Give a bounding box for every leukocyte visible.
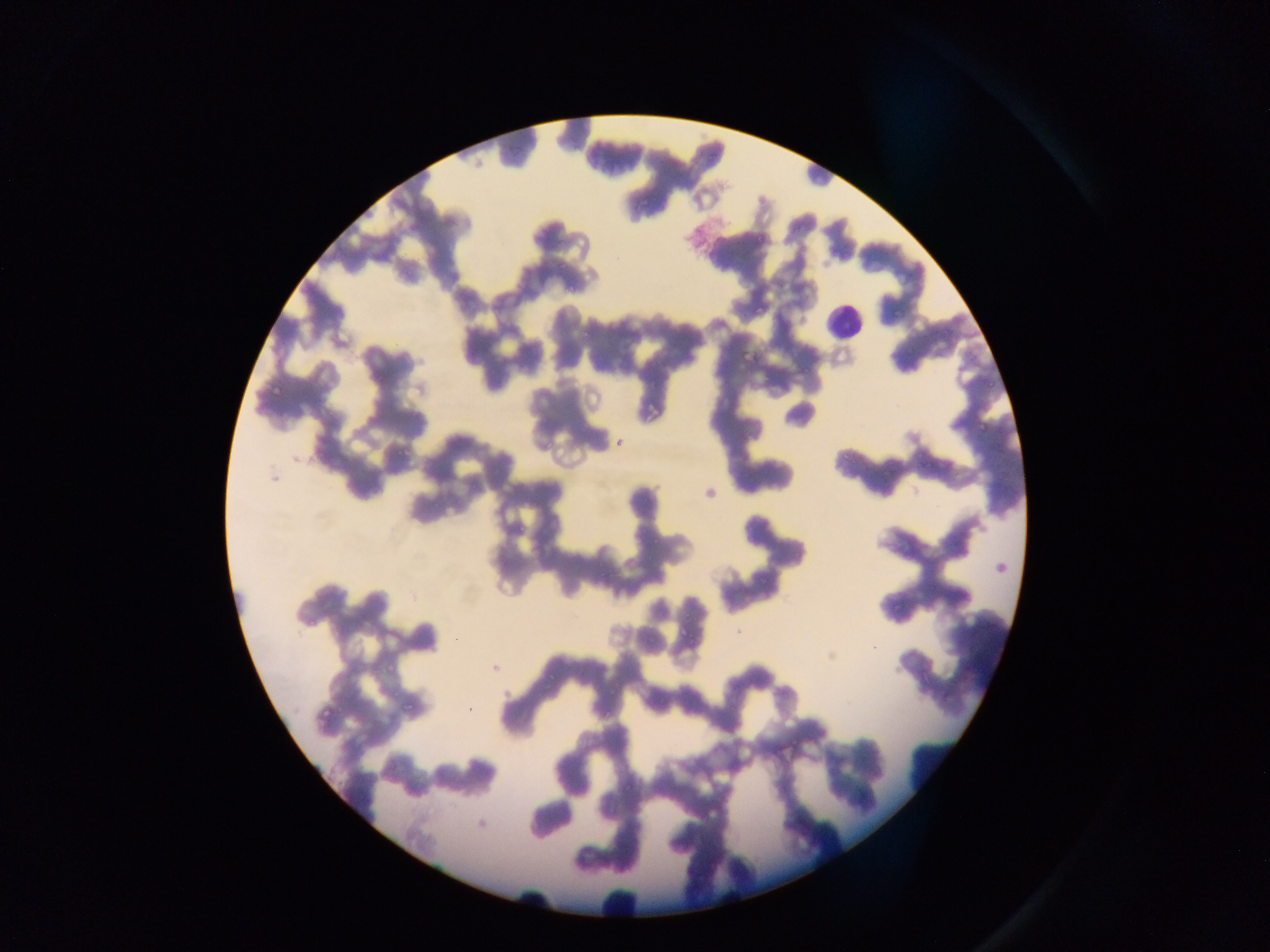
Approximate bounding boxes as [left, top, right, bottom] in pixels.
Leukocytes: [812, 290, 871, 350].

{
  "capture": "mobile-phone photograph through a microscope",
  "country": "Ghana",
  "malaria_parasite_locations": "approximate bounding boxes as [left, top, right, bottom] in pixels: [635, 201, 653, 209], [754, 228, 766, 241], [562, 284, 579, 297], [753, 304, 765, 317], [800, 364, 813, 375], [983, 375, 1003, 392], [972, 420, 987, 433], [837, 444, 848, 464], [514, 524, 529, 536], [757, 571, 774, 590], [681, 606, 694, 619], [684, 627, 701, 653]",
  "preparation": "thin blood film",
  "field_of_view": "single",
  "image_size": "1270×952 pixels"
}